Outline each blood parasite and name the species.
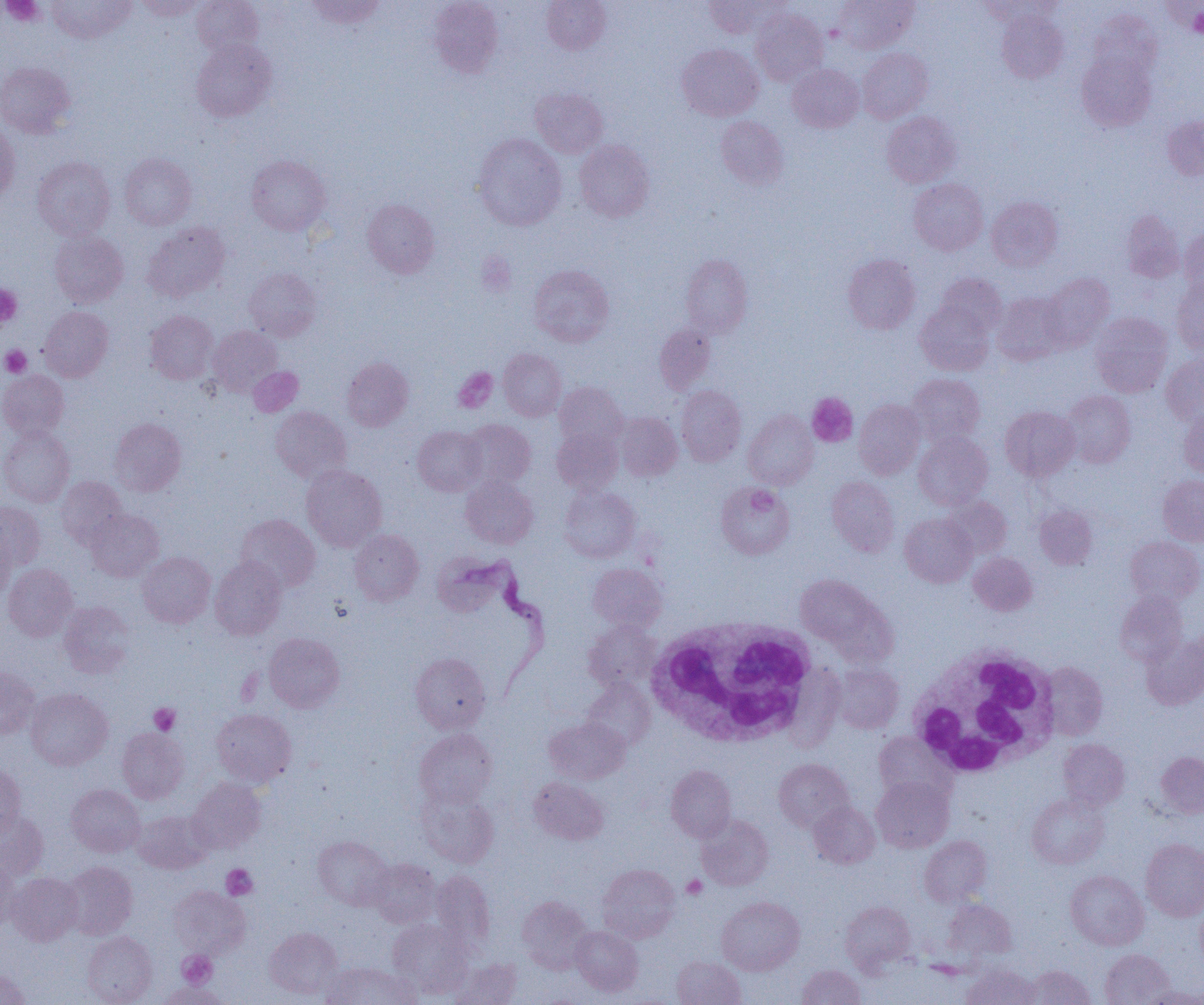
Approximate bounding boxes as (x1,y1)-(x2,y2) corner pairs in pixels.
Trypanosoma brucei: (433,550)-(550,695).
No Plasmodium falciparum, Plasmodium ovale, Plasmodium malariae, Plasmodium vivax, or Babesia divergens observed.

Uninfected red blood cell locations: (47,0)-(135,44), (134,0)-(206,20), (192,0)-(264,57), (306,0)-(386,28), (429,0)-(503,77), (541,0)-(610,53), (703,0)-(786,38), (834,0)-(918,54), (980,0)-(1063,26), (1162,2)-(1203,35), (1088,8)-(1163,83), (751,9)-(828,85), (996,11)-(1068,83), (191,39)-(276,122), (677,44)-(763,121), (857,47)-(932,124), (1076,50)-(1156,132), (0,62)-(76,138), (787,64)-(863,132), (530,87)-(608,157), (882,111)-(960,187), (716,116)-(788,189), (1163,116)-(1204,180), (0,120)-(20,204), (473,133)-(566,230), (574,140)-(654,222), (119,153)-(197,230), (246,154)-(331,236), (33,156)-(115,240), (909,178)-(988,255), (986,196)-(1063,271), (362,199)-(440,278), (1121,210)-(1184,282), (143,222)-(231,302), (1180,226)-(1204,298), (49,230)-(128,308), (680,254)-(753,338), (843,254)-(921,334), (529,264)-(614,346), (244,267)-(321,341), (1040,272)-(1115,352), (935,273)-(1007,339), (1172,277)-(1204,354), (992,292)-(1069,365), (915,301)-(994,375), (39,306)-(113,381), (144,310)-(218,384), (1090,312)-(1172,397), (655,323)-(716,393), (208,325)-(283,396), (498,348)-(566,420), (1161,352)-(1203,425), (342,357)-(413,431), (248,367)-(303,416), (0,370)-(69,440), (907,374)-(986,445), (554,382)-(627,449), (676,386)-(746,466), (1061,390)-(1135,468), (854,399)-(925,479), (270,406)-(351,483), (1000,406)-(1079,480), (1179,407)-(1204,477), (743,410)-(818,489), (615,412)-(682,481), (109,418)-(186,496), (461,420)-(535,489), (0,426)-(74,507), (413,426)-(486,496), (552,427)-(623,494), (913,432)-(993,510), (302,465)-(387,551), (1158,475)-(1204,545), (56,476)-(127,549), (460,476)-(538,548), (827,476)-(899,556), (716,482)-(794,559), (559,486)-(640,562), (942,496)-(1012,559), (0,501)-(45,569), (1035,505)-(1098,569), (86,509)-(163,581), (900,513)-(977,587), (236,514)-(320,592), (0,528)-(15,600), (349,529)-(424,605), (1125,536)-(1204,604), (137,552)-(215,627), (968,552)-(1037,615), (210,557)-(287,639), (3,563)-(78,641), (588,563)-(666,633), (795,574)-(883,651), (1115,591)-(1187,665), (58,601)-(135,678), (583,620)-(661,691), (264,632)-(344,712), (1141,633)-(1204,709), (410,652)-(491,733), (1041,662)-(1108,740), (832,664)-(903,733), (0,667)-(40,739), (581,679)-(655,749), (26,688)-(113,770), (211,709)-(296,787), (544,716)-(630,784), (117,727)-(189,803), (414,728)-(497,808), (874,732)-(955,804), (1058,738)-(1130,811), (1156,751)-(1204,818), (774,758)-(854,832), (0,764)-(26,838), (666,765)-(736,842), (187,777)-(265,853), (529,777)-(608,845), (871,777)-(953,852), (66,784)-(145,857), (417,788)-(500,869), (1027,793)-(1109,869), (808,802)-(880,868), (132,810)-(213,874), (0,811)-(48,881), (696,814)-(773,890), (313,836)-(393,910), (920,836)-(992,906), (1141,839)-(1204,920), (0,858)-(20,932), (367,859)-(440,928), (61,861)-(137,939), (598,864)-(680,942), (430,870)-(495,951), (1065,870)-(1148,949), (8,872)-(84,945), (169,886)-(250,958), (517,895)-(593,973), (717,896)-(805,975), (943,899)-(1016,960), (840,901)-(915,971), (1195,901)-(1204,971), (387,918)-(472,998), (571,926)-(643,996), (264,927)-(342,999), (82,931)-(157,1004), (1100,949)-(1174,1005), (672,956)-(746,1005), (449,957)-(521,1005), (322,961)-(418,1005), (961,964)-(1040,1005), (796,965)-(865,1005), (1022,965)-(1095,1005), (0,969)-(30,1005), (157,982)-(229,1005), (1144,987)-(1204,1005). White blood cell locations: (646,617)-(822,747), (907,644)-(1061,778). Platelet locations: (1,0)-(45,26), (1188,6)-(1203,38), (0,284)-(22,327), (1,345)-(32,377), (453,367)-(497,412), (806,393)-(858,446), (149,702)-(180,735), (222,864)-(258,900), (682,875)-(707,899), (177,950)-(217,989). Slide-level diagnosis: Trypanosoma brucei. 1000x magnification. Image is 1204×1005 pixels. Thin blood film. One field of a larger specimen. Optical microscopy.